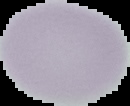

image size = 130×106 pixels
preparation = thin blood smear
image type = segmented cell region on a black background
result = negative for malaria parasites